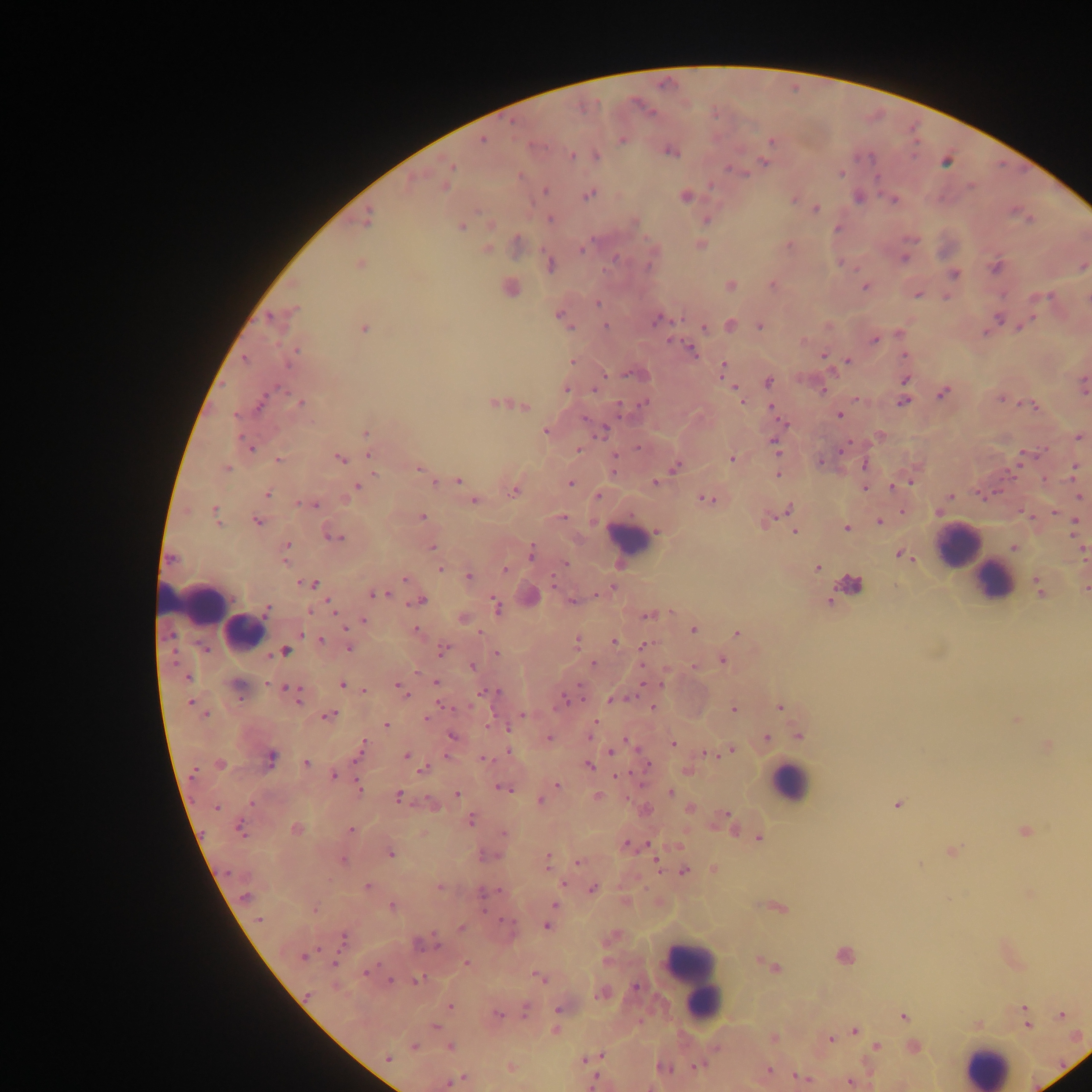

Approximate centers as x y in pixels. Leukocyte locations: 630 537; 957 546; 1000 584; 191 595; 243 630; 788 782; 697 984; 992 1059. Malaria parasite locations: 652 113; 622 139; 482 141; 771 141; 668 152; 596 155; 573 156; 763 161; 453 167; 727 167; 745 173; 841 173; 521 176; 710 185; 445 186; 971 187; 544 190; 590 194; 685 197; 795 199; 894 200; 816 208; 476 211; 1012 211; 550 218; 706 220; 489 224; 461 227; 487 249; 581 249; 903 256; 614 258; 359 264; 997 266; 991 268; 855 269; 954 274; 771 284; 730 285; 865 287; 917 295; 1051 296; 946 297; 1035 298; 597 303; 294 309; 271 316; 560 317; 999 317; 1034 318; 655 320; 605 325; 1018 325; 759 326; 704 327; 363 329; 985 333; 875 338; 690 347; 823 355; 905 355; 244 357; 849 359; 571 362; 723 365; 721 371; 833 372; 627 374; 605 376; 905 380; 769 381; 599 382; 1083 386; 276 387; 734 387; 566 390; 594 391; 823 391; 943 393; 855 398; 1000 399; 741 401; 902 402; 261 403; 302 403; 493 403; 643 403; 1019 403; 1034 404; 525 405; 618 406; 771 406; 839 415; 235 416; 583 418; 781 422; 364 432; 545 432; 602 432; 1079 437; 850 441; 774 446; 845 447; 578 448; 251 449; 1042 449; 840 452; 1021 453; 369 454; 615 455; 731 458; 277 459; 339 460; 821 461; 863 465; 1074 466; 228 468; 418 469; 669 472; 373 474; 458 482; 569 483; 655 483; 911 483; 434 484; 358 486; 864 487; 890 487; 513 491; 267 494; 981 494; 704 496; 951 496; 1080 497; 473 501; 296 502; 316 506; 788 508; 904 512; 938 512; 1055 512; 563 515; 422 516; 768 518; 1075 520; 257 521; 879 522; 847 527; 795 531; 332 536; 340 537; 289 544; 431 548; 530 550; 900 553; 910 558; 285 562; 565 563; 817 568; 440 569; 505 570; 468 577; 405 579; 553 580; 315 582; 299 583; 308 583; 612 588; 387 594; 596 595; 373 596; 326 599; 574 601; 413 603; 497 605; 310 611; 672 611; 266 612; 333 612; 648 617; 364 621; 416 628; 344 629; 692 630; 480 633; 738 633; 301 634; 321 638; 578 642; 615 642; 642 645; 349 648; 443 649; 206 650; 496 651; 268 656; 174 661; 593 663; 642 665; 171 666; 472 666; 416 673; 188 679; 434 681; 267 684; 643 684; 344 686; 399 686; 580 686; 284 687; 364 692; 482 692; 498 692; 407 694; 565 695; 628 697; 619 698; 241 699; 582 699; 190 702; 298 703; 438 704; 781 706; 652 707; 456 708; 732 708; 208 714; 334 714; 522 715; 327 716; 426 719; 1016 719; 597 720; 385 725; 488 725; 506 728; 452 737; 549 737; 590 737; 768 737; 624 740; 364 743; 673 744; 731 748; 507 751; 609 753; 703 753; 710 753; 360 755; 446 755; 271 756; 406 756; 481 759; 306 763; 591 765; 647 765; 424 769; 333 775; 617 776; 358 783; 556 785; 359 788; 501 789; 671 793; 457 794; 398 796; 598 796; 540 800; 250 801; 427 801; 415 802; 897 804; 216 807; 689 808; 727 814; 471 818; 240 828; 297 829; 351 830; 1026 830; 502 834; 760 837; 626 845; 952 852; 391 854; 549 857; 343 860; 656 860; 577 864; 919 865; 548 868; 226 873; 563 883; 366 885; 593 887; 440 888; 498 890; 1030 894; 246 896; 949 898; 555 904; 392 906; 485 909; 316 910; 498 917; 262 920; 501 920; 459 926; 547 926; 432 932; 434 936; 345 939; 341 944; 438 947; 319 948; 305 954; 302 957; 467 963; 379 964; 333 965; 365 973; 539 977; 389 979; 415 979; 636 987; 307 994; 597 997; 449 1006; 1024 1006; 526 1009; 557 1009; 498 1015; 1059 1015; 905 1017; 435 1026; 1028 1026; 556 1028; 853 1031; 830 1039; 877 1046; 413 1047; 603 1055; 587 1059; 388 1060; 692 1066; 510 1067; 769 1069; 796 1075; 463 1076; 596 1077; 850 1082; 447 1084; 589 1086. Mobile-phone photograph taken through the microscope. Thick blood smear. Sample from Ghana. Single field of view. Image is 1092×1092 pixels.